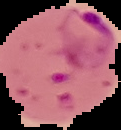 Image is 121×130 pixels. From a thin blood film. Malaria status: parasitized. Segmented cell region on a black background.